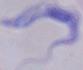

Summary:
  - Modality: photomicrograph
  - Magnification: 1000x
  - Identification: trypanosome